Evaluate for parasitized red blood cells.
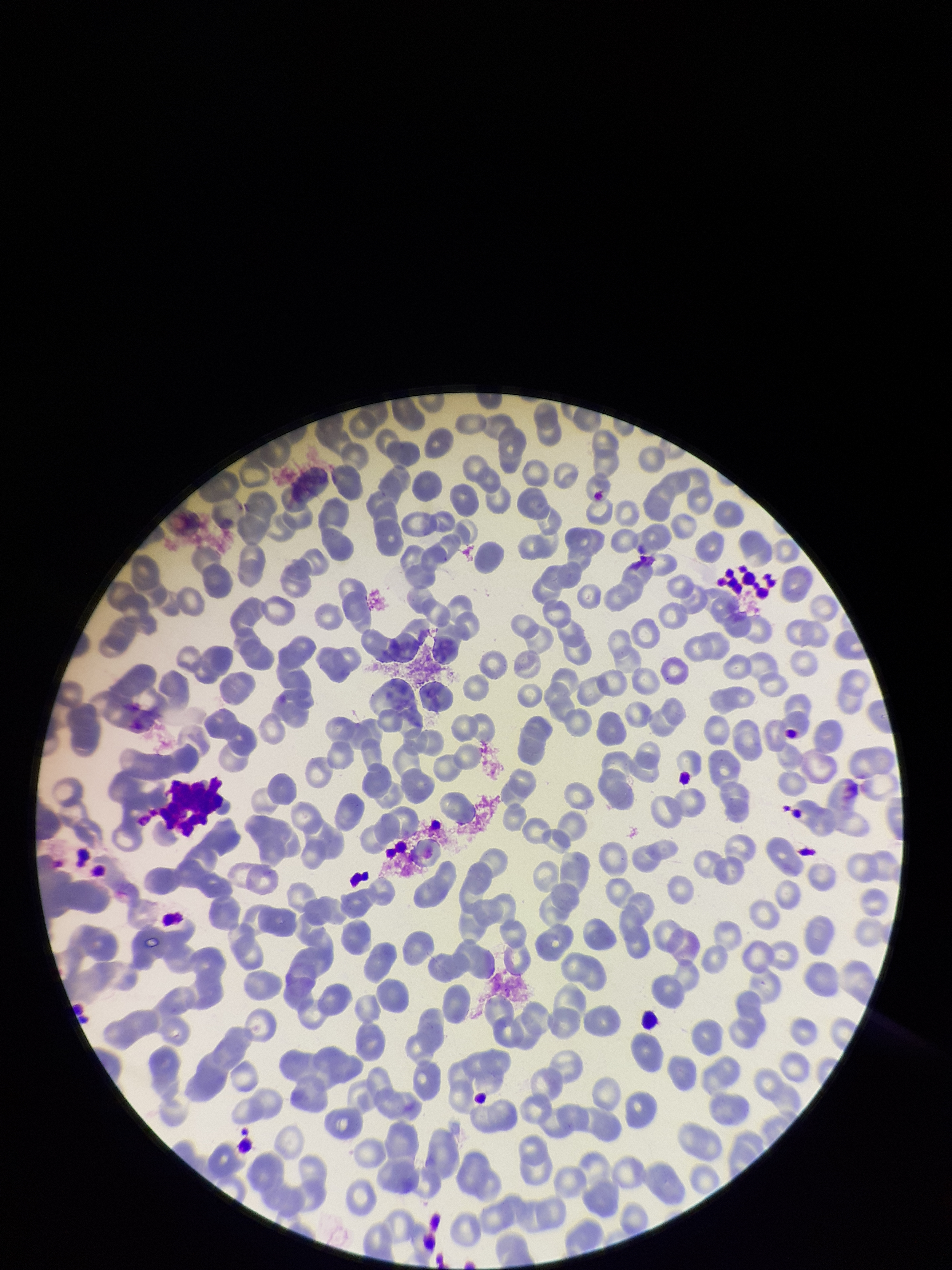

None detected.

Preparation: thin smear. Giemsa stain. Red blood cell count: 268. Image is 952×1270 pixels. Parasitized red blood cell count: 0. Single field of view. Patient malaria status: negative. Smartphone photograph taken through the eyepiece of a microscope.